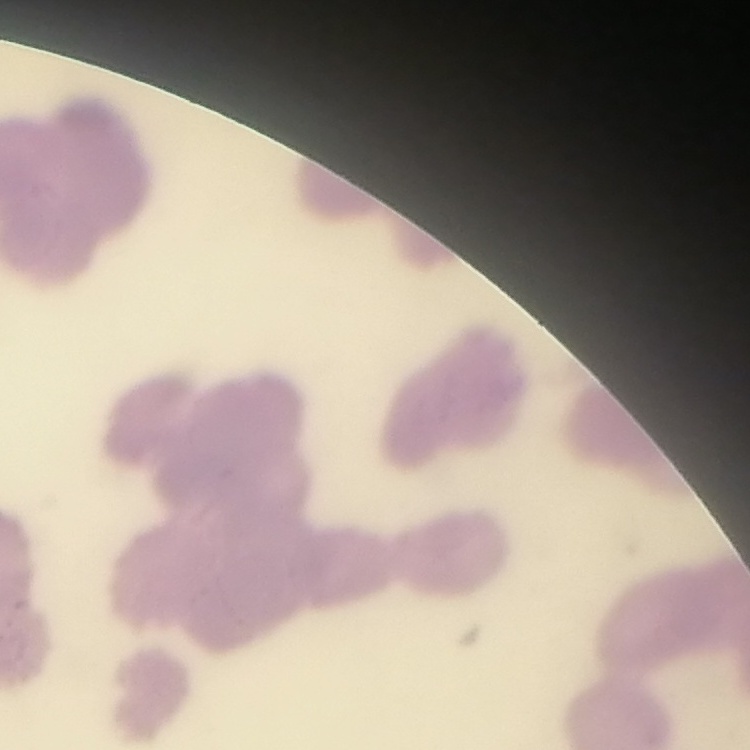
Summary:
  - Erythrocyte morphology: rouleaux formation
  - Image type: square crop of a larger photomicrograph
  - Preparation: thin blood smear
  - Stain: Field's or Giemsa